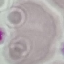

{
  "result": "negative for malaria parasites",
  "capture": "smartphone through the microscope eyepiece",
  "preparation": "thin smear",
  "image_type": "cell patch, automatically extracted from a larger field of view and resized to 64 × 64 pixels",
  "stain": "Giemsa"
}